Locate every Plasmodium parasite.
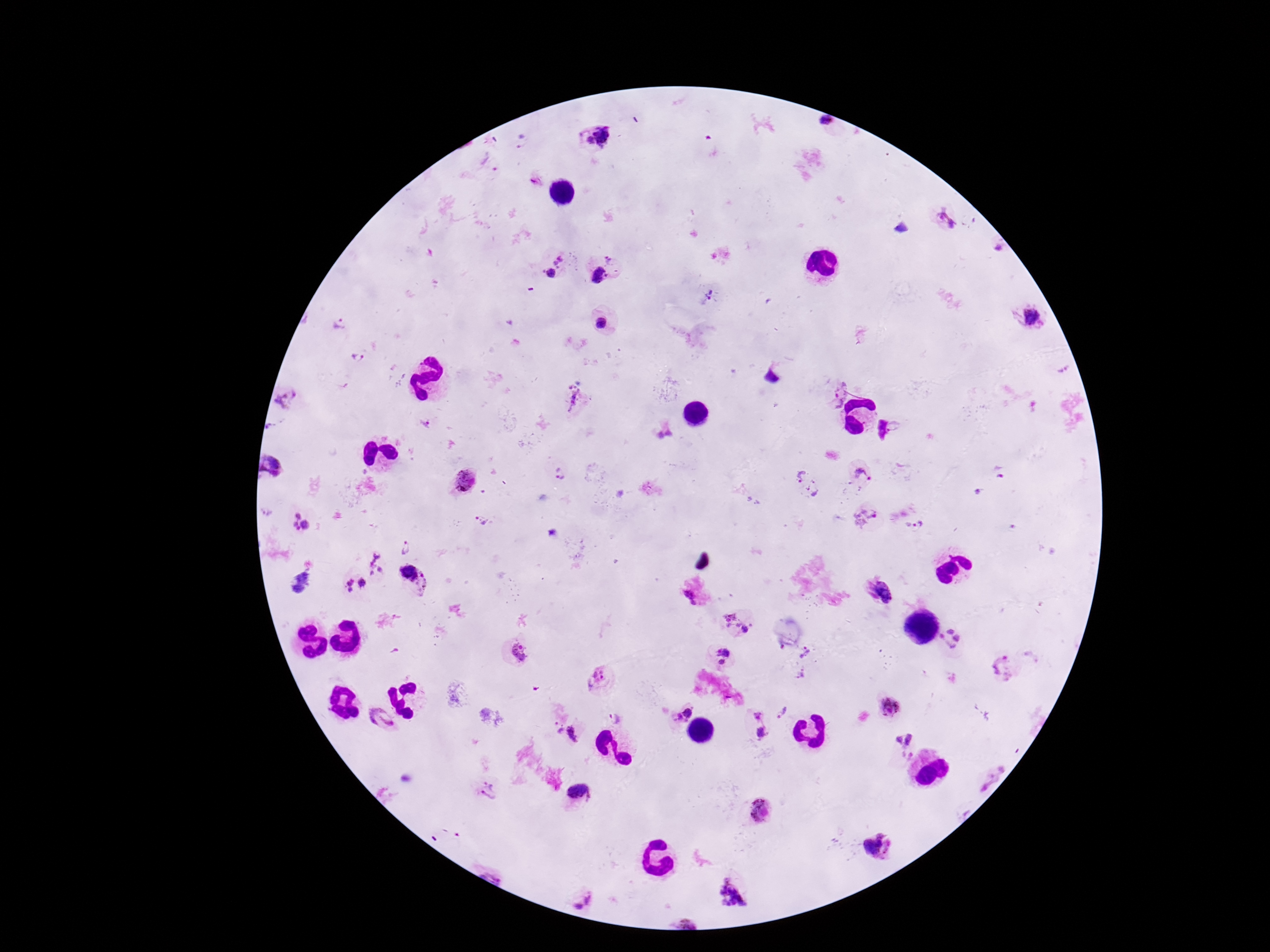
Approximate centers as [x, y] in pixels.
Plasmodium parasites: [825, 122], [595, 136], [946, 218], [997, 247], [612, 259], [560, 260], [549, 274], [599, 275], [710, 293], [602, 323], [340, 325], [357, 357], [837, 393], [577, 398], [285, 402], [272, 425], [425, 426], [896, 428], [270, 468], [561, 475], [863, 475], [468, 481], [808, 487], [265, 514], [866, 517], [484, 521], [918, 526], [300, 527], [408, 545], [379, 566], [418, 580], [297, 586], [351, 586], [881, 594], [690, 596], [739, 621], [952, 639], [519, 651], [808, 653], [722, 657], [1003, 667], [801, 674], [598, 679], [891, 707], [681, 711], [783, 712], [757, 716], [613, 718], [379, 721], [762, 733], [566, 734], [903, 741], [486, 791], [581, 793], [759, 810], [878, 847], [732, 897], [577, 898].

Summary:
  - Preparation: thick blood smear
  - Patient malaria status: infected
  - Image size: 1270×952 pixels
  - Capture: smartphone camera through the microscope eyepiece
  - Stain: Giemsa
  - Field of view: single
  - Magnification: 100x